Point out each Plasmodium parasite and each leukocyte.
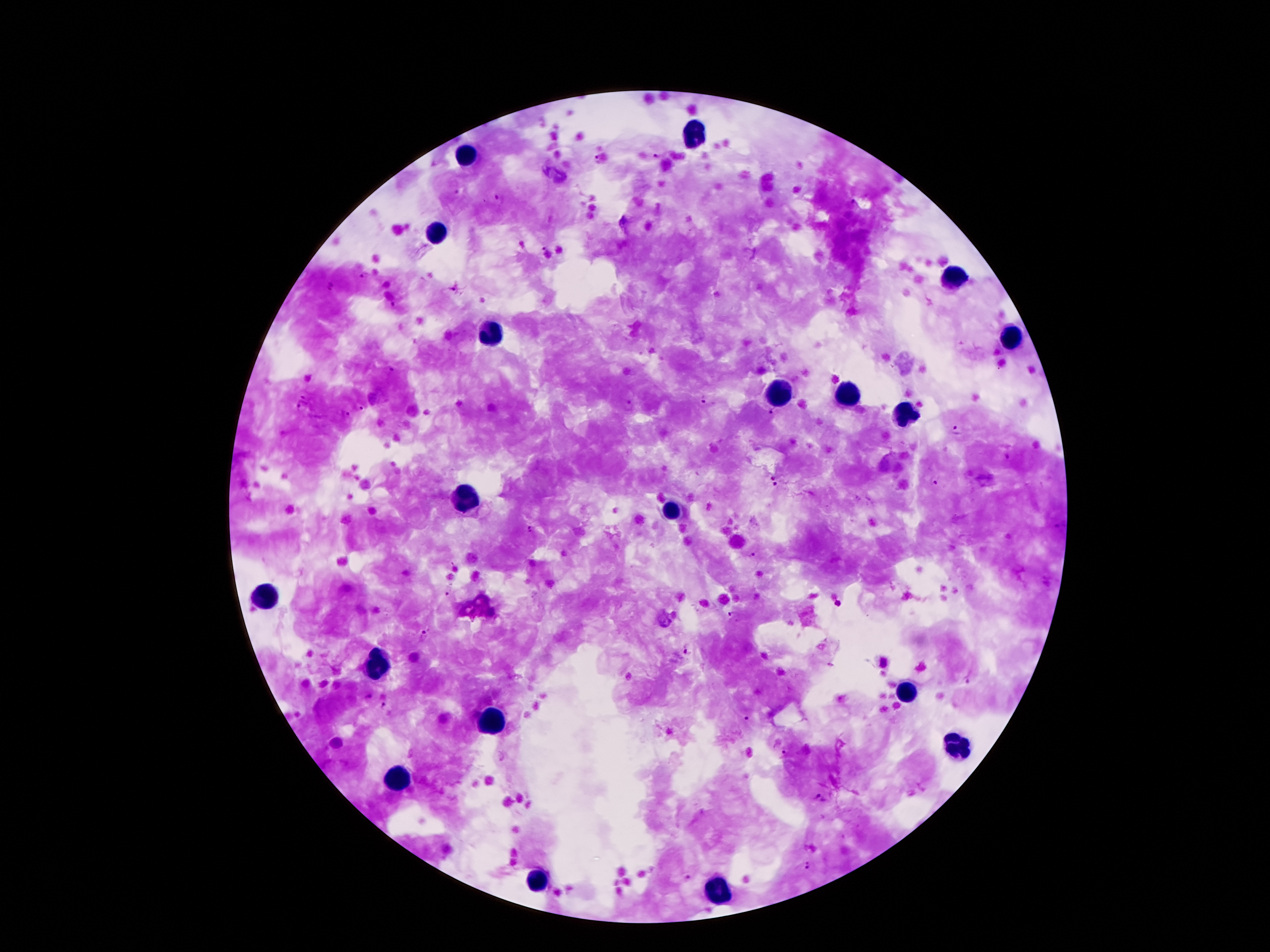
Approximate object centers, in pixels from the top-left corner.
Plasmodium parasites: (x=657, y=156), (x=597, y=160), (x=457, y=189), (x=497, y=196), (x=852, y=203), (x=542, y=247), (x=366, y=275), (x=332, y=287), (x=455, y=290), (x=393, y=304), (x=393, y=369), (x=705, y=400), (x=303, y=405), (x=361, y=407), (x=770, y=412), (x=344, y=414), (x=956, y=428), (x=773, y=478), (x=935, y=479), (x=775, y=486), (x=529, y=529), (x=751, y=554), (x=445, y=593), (x=838, y=604), (x=732, y=613), (x=423, y=634), (x=688, y=649), (x=968, y=682), (x=371, y=697), (x=385, y=705), (x=748, y=718), (x=782, y=753), (x=815, y=796), (x=810, y=865), (x=686, y=878).
Leukocytes: (x=692, y=135), (x=468, y=156), (x=433, y=237), (x=954, y=277), (x=489, y=334), (x=1012, y=343), (x=778, y=395), (x=847, y=400), (x=906, y=415), (x=468, y=497), (x=671, y=509), (x=269, y=594), (x=379, y=667), (x=901, y=693), (x=489, y=725), (x=957, y=748), (x=402, y=782), (x=535, y=886), (x=720, y=893).

Patient malaria status: positive for Plasmodium falciparum. 100x magnification. Smartphone photograph taken through the microscope eyepiece. One field from this slide. Giemsa stain. Thick blood smear. Image is 1270×952 pixels.